Name the parasite shown.
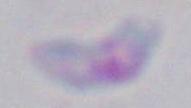
This is Toxoplasma gondii.

1000x magnification. Micrograph.